Assess this cell for malaria.
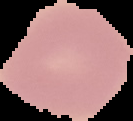
Uninfected.

Summary:
  - Preparation: thin blood smear
  - Image size: 133×121 pixels
  - Image type: segmented cell region with the area outside set to black